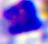
Photomicrograph. A white blood cell is shown. 400x magnification.